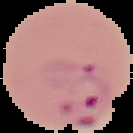
malaria_status: parasitized
preparation: thin blood smear
image_type: cell region segmented out of the field of view; surrounding area masked to black
image_size: 133×133 pixels